Classify this cell by malaria status.
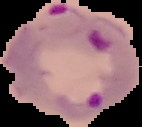
Parasitized.

From a thin blood film. Cell region segmented out of the field of view; the surrounding area is masked to black. Image is 142×127 pixels.